Report the malaria status of this cell.
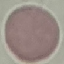
Uninfected.

Summary:
  - Stain: Giemsa
  - Capture: smartphone through the microscope eyepiece
  - Image type: cell patch, automatically extracted from a larger field of view and resized to 64 × 64 pixels
  - Preparation: thin smear